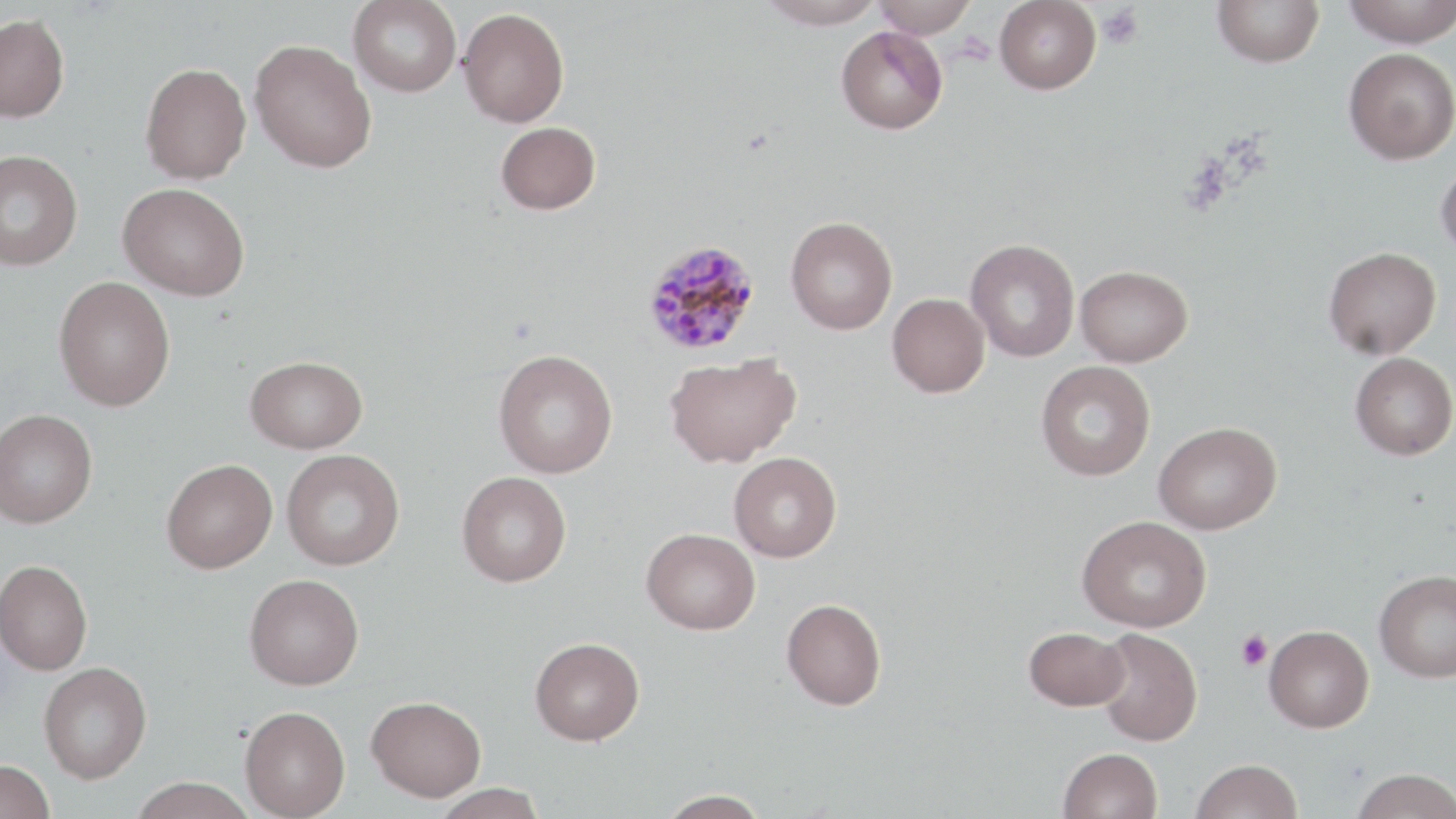
Approximate bounding boxes as named x1/y1/x2/y2 corners in pixels. Plasmodium malariae-infected red blood cell locations: (x1=641, y1=239, x2=760, y2=357). Platelet locations: (x1=1099, y1=5, x2=1143, y2=49), (x1=1236, y1=629, x2=1272, y2=671). Uninfected red blood cell locations: (x1=348, y1=0, x2=461, y2=97), (x1=757, y1=0, x2=885, y2=29), (x1=873, y1=0, x2=977, y2=38), (x1=994, y1=0, x2=1102, y2=94), (x1=1213, y1=0, x2=1324, y2=67), (x1=1343, y1=0, x2=1456, y2=48), (x1=458, y1=7, x2=569, y2=127), (x1=0, y1=13, x2=70, y2=123), (x1=836, y1=26, x2=948, y2=134), (x1=250, y1=39, x2=377, y2=173), (x1=1344, y1=48, x2=1456, y2=164), (x1=140, y1=62, x2=251, y2=184), (x1=496, y1=121, x2=601, y2=215), (x1=0, y1=150, x2=83, y2=270), (x1=1436, y1=160, x2=1456, y2=260), (x1=118, y1=182, x2=250, y2=300), (x1=786, y1=216, x2=898, y2=334), (x1=966, y1=239, x2=1079, y2=362), (x1=1323, y1=246, x2=1441, y2=360), (x1=1076, y1=265, x2=1193, y2=367), (x1=54, y1=276, x2=176, y2=411), (x1=887, y1=293, x2=990, y2=398), (x1=493, y1=348, x2=618, y2=478), (x1=665, y1=352, x2=801, y2=468), (x1=1350, y1=352, x2=1456, y2=460), (x1=244, y1=355, x2=368, y2=453), (x1=1036, y1=360, x2=1156, y2=481), (x1=0, y1=408, x2=98, y2=528), (x1=1153, y1=421, x2=1281, y2=534), (x1=281, y1=449, x2=404, y2=570), (x1=729, y1=452, x2=841, y2=561), (x1=161, y1=458, x2=277, y2=573), (x1=457, y1=471, x2=571, y2=586), (x1=1077, y1=515, x2=1211, y2=632), (x1=641, y1=527, x2=760, y2=634), (x1=0, y1=559, x2=92, y2=675), (x1=1374, y1=569, x2=1456, y2=682), (x1=244, y1=574, x2=364, y2=690), (x1=781, y1=598, x2=887, y2=710), (x1=1264, y1=625, x2=1374, y2=732), (x1=1024, y1=626, x2=1129, y2=710), (x1=1095, y1=628, x2=1202, y2=746), (x1=530, y1=636, x2=645, y2=745), (x1=39, y1=662, x2=152, y2=783), (x1=366, y1=695, x2=486, y2=801), (x1=239, y1=705, x2=350, y2=819), (x1=1058, y1=747, x2=1162, y2=819), (x1=0, y1=759, x2=56, y2=819), (x1=1191, y1=759, x2=1303, y2=819), (x1=1350, y1=768, x2=1456, y2=819), (x1=127, y1=777, x2=257, y2=819), (x1=429, y1=783, x2=547, y2=819), (x1=654, y1=789, x2=772, y2=818). Slide-level diagnosis: Plasmodium malariae. Thin blood smear. May-Grünwald-Giemsa-stained preparation. Optical microscopy. 1000x magnification. Image is 1456×819 pixels. One field of a larger specimen.